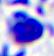
Photomicrograph. A leukocyte is shown. Captured at 400x magnification.